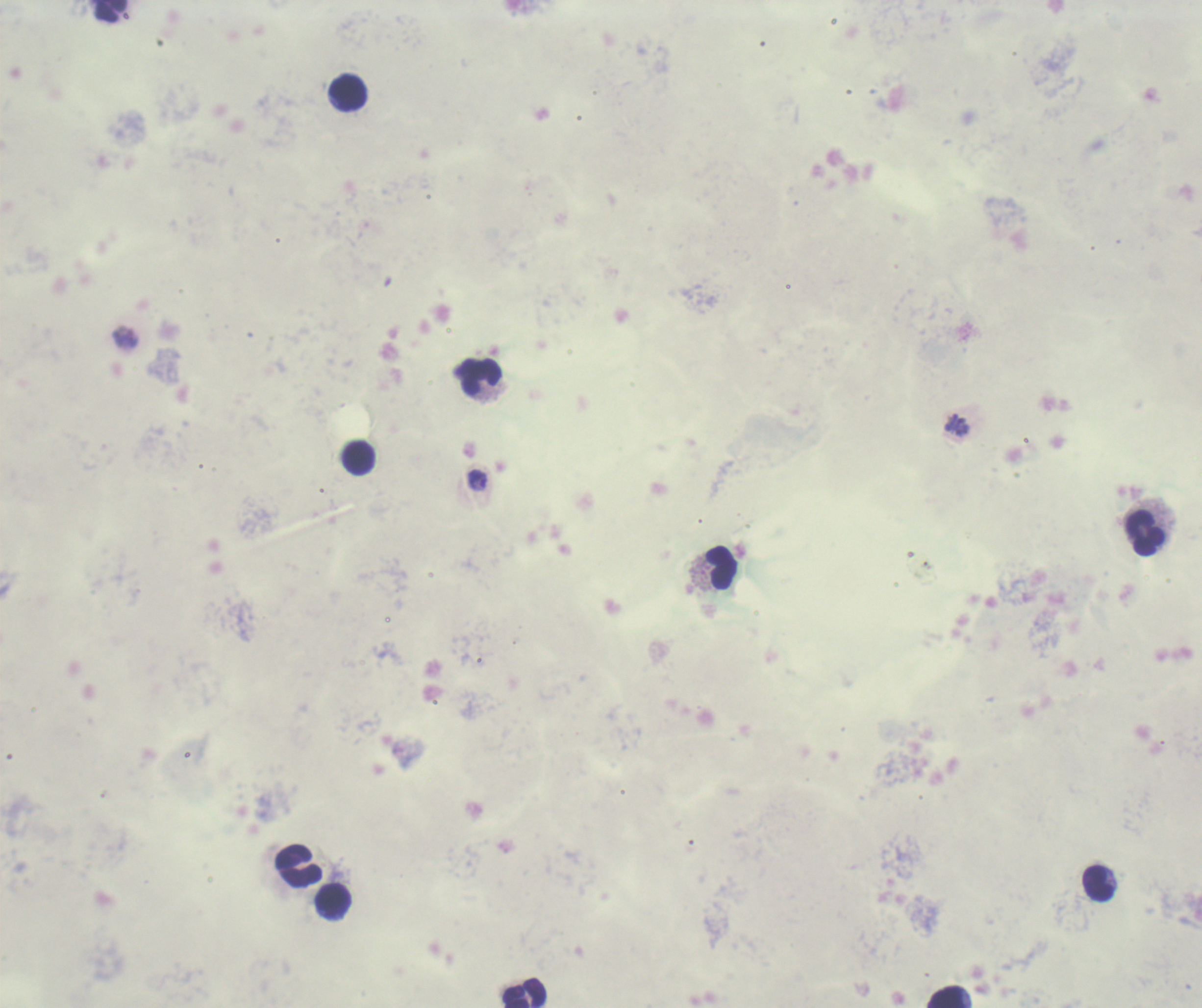

Approximate centers as (x, y) in pixels. Trophozoite locations: (477, 480). Leukocyte locations: (111, 11), (348, 93), (479, 377), (358, 458), (1145, 532), (721, 568), (298, 867), (1098, 883), (334, 901), (524, 993), (948, 997). Result: Plasmodium parasites identified. Captured at 100x magnification. Thick blood smear. Background quality: unsatisfactory. Coloration quality: bad. Romanowsky stain. Image is 1202×1008 pixels. Previously used in a real diagnosis. One field from this slide.